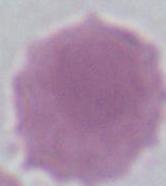
Micrograph. An erythrocyte is shown. Captured at 1000x magnification.